Locate and identify every blood parasite.
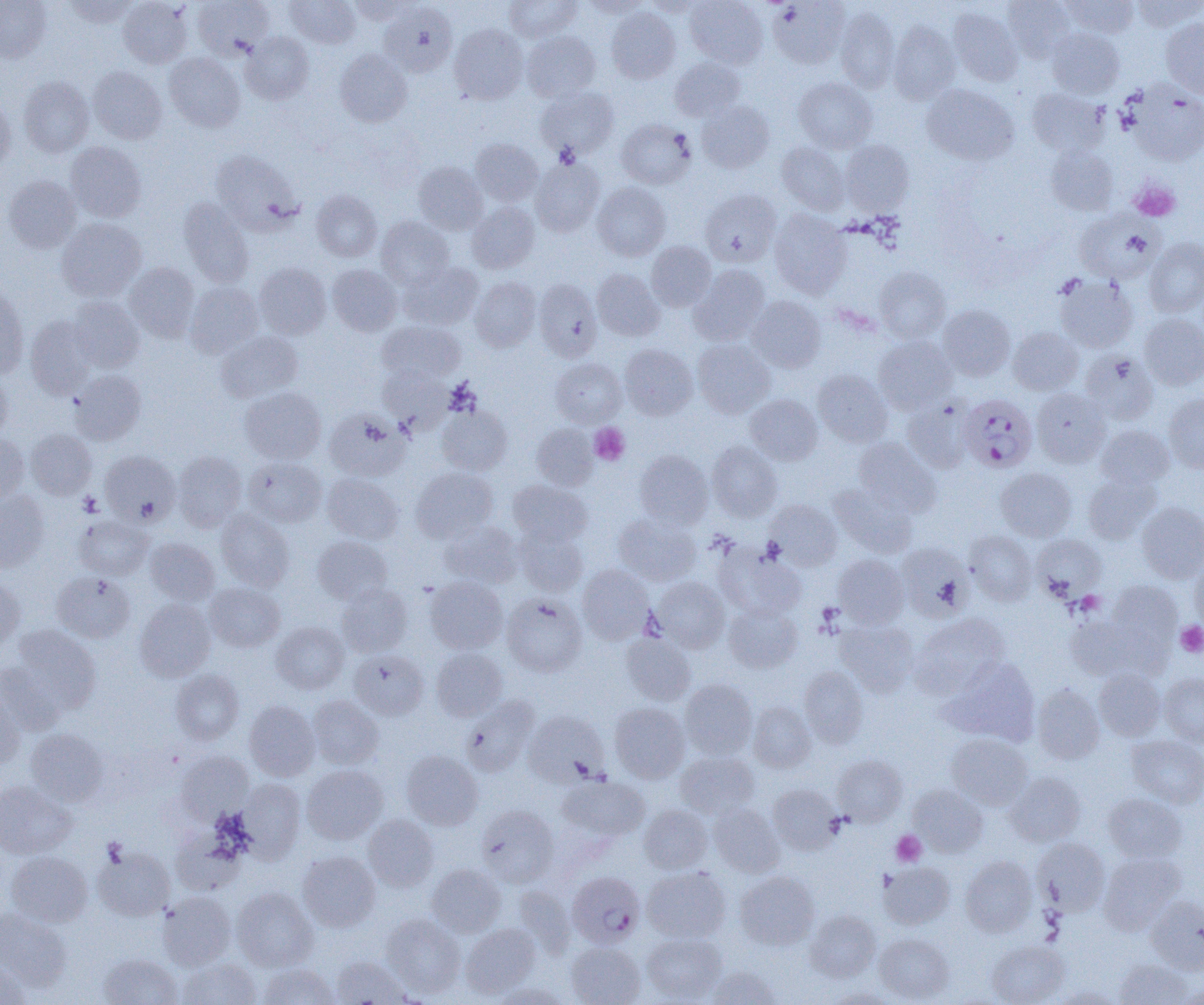
Approximate bounding boxes as [x1, y1, x2, y2] in pixels.
Plasmodium falciparum-infected red blood cells (subset): [958, 394, 1037, 472].
No Plasmodium ovale, Plasmodium malariae, Plasmodium vivax, Babesia divergens, or Trypanosoma brucei observed.

Uninfected red blood cell locations (subset): [0, 0, 52, 63], [63, 0, 140, 27], [118, 0, 192, 68], [192, 0, 273, 60], [285, 0, 361, 49], [348, 0, 418, 23], [505, 0, 582, 42], [582, 0, 650, 19], [643, 0, 706, 16], [685, 0, 768, 69], [1002, 0, 1075, 62], [1062, 0, 1139, 39], [1130, 0, 1203, 32], [768, 1, 850, 68], [379, 3, 457, 77], [835, 6, 900, 93], [948, 6, 1023, 85], [606, 7, 680, 83], [1161, 18, 1204, 98], [888, 21, 960, 104], [449, 24, 528, 104], [1047, 28, 1124, 99], [521, 31, 600, 102], [241, 32, 314, 104], [335, 49, 412, 127], [164, 52, 245, 131], [670, 57, 745, 121], [88, 66, 167, 144], [18, 76, 94, 158], [793, 77, 877, 153], [922, 84, 1018, 165], [1126, 84, 1204, 166], [536, 86, 619, 160], [1027, 88, 1108, 156], [0, 97, 15, 173], [697, 101, 774, 173], [617, 119, 696, 189], [470, 139, 543, 206], [839, 140, 915, 216], [65, 142, 147, 222], [777, 142, 849, 215], [1046, 145, 1118, 216], [210, 148, 300, 232], [530, 157, 604, 236], [413, 162, 487, 234], [3, 176, 82, 253], [592, 182, 671, 261], [311, 190, 382, 262], [700, 190, 781, 267], [179, 198, 254, 288], [467, 202, 539, 273], [770, 210, 851, 298], [1075, 211, 1161, 283], [376, 216, 454, 289], [57, 218, 146, 302], [1144, 238, 1204, 318], [646, 241, 716, 311], [399, 262, 484, 330], [125, 263, 200, 342], [254, 263, 331, 339], [327, 264, 403, 336], [690, 264, 770, 344], [874, 267, 950, 343], [592, 269, 665, 341], [1056, 276, 1138, 353], [470, 277, 541, 352], [534, 278, 602, 362], [186, 282, 263, 358], [0, 286, 28, 378], [746, 296, 826, 373], [68, 297, 145, 372], [938, 304, 1015, 380], [1139, 313, 1204, 390], [26, 315, 97, 399], [377, 320, 464, 384], [1008, 327, 1083, 395], [215, 330, 303, 402], [873, 336, 956, 414], [693, 339, 775, 417], [620, 344, 698, 419], [1080, 350, 1158, 424], [551, 358, 626, 426], [378, 365, 452, 432], [70, 370, 146, 444], [813, 370, 892, 446], [0, 371, 12, 441], [240, 387, 326, 464], [1032, 388, 1111, 468], [1164, 393, 1204, 473], [745, 395, 822, 465], [903, 399, 973, 473], [437, 405, 512, 476], [325, 408, 409, 481], [532, 423, 598, 490], [1096, 424, 1173, 489], [26, 429, 97, 499], [0, 433, 29, 504], [853, 437, 939, 516], [708, 441, 783, 522], [101, 450, 180, 526], [173, 450, 247, 532], [635, 450, 713, 528], [244, 457, 328, 527], [411, 467, 498, 544], [996, 468, 1077, 541], [323, 473, 404, 544], [1083, 473, 1162, 543], [508, 480, 592, 546], [831, 481, 918, 558], [0, 490, 49, 571], [766, 499, 842, 570], [1136, 501, 1204, 582], [216, 509, 295, 591], [614, 513, 701, 586], [74, 515, 153, 580], [439, 521, 523, 588], [515, 527, 587, 597], [964, 530, 1037, 605], [1031, 534, 1106, 599], [312, 536, 392, 604], [145, 537, 219, 605], [895, 541, 974, 621], [715, 546, 806, 619], [833, 555, 909, 629], [1190, 558, 1204, 632], [577, 564, 653, 644], [53, 572, 135, 643], [0, 577, 25, 649], [425, 577, 508, 653], [652, 577, 730, 652], [1108, 580, 1182, 650], [205, 582, 285, 652], [335, 583, 413, 657], [502, 593, 587, 676], [134, 599, 215, 682], [724, 603, 802, 673], [911, 613, 1009, 698], [1065, 613, 1160, 681], [836, 619, 918, 695], [271, 621, 349, 694], [11, 625, 102, 714], [621, 633, 696, 705], [431, 648, 507, 721], [349, 649, 428, 719], [944, 658, 1041, 745], [0, 662, 64, 734], [800, 665, 868, 748], [1094, 668, 1165, 740], [170, 669, 243, 745], [1159, 672, 1204, 747], [680, 679, 757, 758], [1032, 683, 1104, 764], [0, 687, 25, 769], [307, 695, 383, 769], [461, 695, 539, 777], [244, 700, 319, 780], [747, 701, 816, 772], [610, 702, 690, 783], [524, 710, 610, 787], [25, 728, 109, 806], [947, 734, 1033, 809], [1127, 735, 1204, 808], [401, 750, 483, 830], [176, 751, 253, 823], [676, 751, 759, 818], [832, 755, 907, 826], [302, 765, 387, 844], [1006, 771, 1086, 847], [557, 777, 650, 843], [238, 778, 306, 863], [0, 780, 77, 859], [768, 783, 842, 855], [908, 784, 988, 857], [1103, 793, 1186, 862], [708, 802, 784, 877], [476, 804, 560, 887], [639, 805, 712, 874], [363, 814, 439, 892], [172, 826, 248, 896], [1034, 838, 1110, 914], [93, 845, 175, 921], [6, 851, 93, 927], [298, 851, 380, 932], [1099, 852, 1184, 934], [961, 856, 1037, 936], [879, 863, 955, 929], [426, 864, 506, 937], [642, 867, 730, 942], [735, 871, 819, 950], [231, 887, 318, 971], [158, 892, 236, 970], [1145, 895, 1204, 973], [0, 907, 72, 990], [805, 909, 880, 982], [381, 913, 465, 997], [461, 924, 540, 998], [642, 931, 726, 1003], [874, 933, 954, 1003], [987, 940, 1069, 1005], [566, 942, 645, 1005], [97, 954, 183, 1004], [332, 957, 410, 1004], [178, 958, 262, 1005], [1115, 958, 1192, 1004], [0, 960, 31, 1005], [258, 963, 339, 1005], [704, 965, 781, 1005], [489, 981, 571, 1004], [1054, 985, 1122, 1004], [1175, 985, 1204, 1003], [825, 987, 899, 1004]. Platelet locations: [1130, 181, 1180, 221], [589, 423, 629, 465], [78, 492, 102, 517], [1176, 622, 1204, 657], [891, 830, 926, 866]. Slide-level diagnosis: Plasmodium falciparum. One field of a larger specimen. 1000x magnification. Thin blood smear. Image is 1204×1005 pixels. Light microscopy.